Assess this cell for malaria.
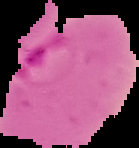

Parasitized.

Image is 139×148 pixels. Segmented cell region on a black background. From a thin blood film.